Report the malaria status of this cell.
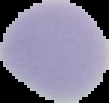
Uninfected.

image type = segmented cell region with the area outside set to black
preparation = thin blood film
image size = 109×103 pixels